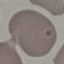 Result: no malaria parasites seen. Thin blood film. Cell patch, automatically extracted from a larger field of view and resized to 64 × 64 pixels. Giemsa-stained preparation. Photographed with a smartphone camera at the microscope eyepiece.